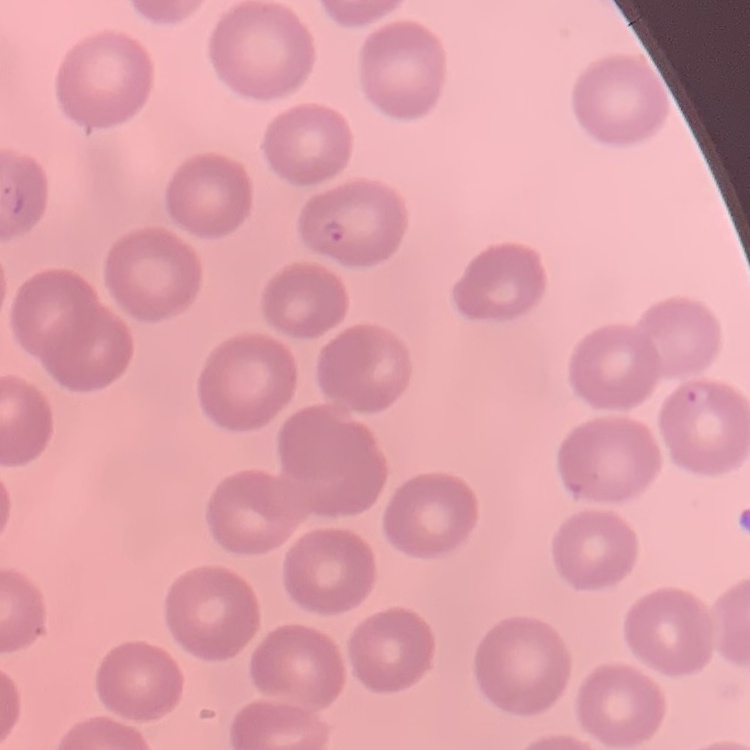

The red blood cells show no rouleaux formation. One tile cut from a larger photomicrograph. Thin blood smear. Stained with either Field's or Giemsa.